Give the preparation type.
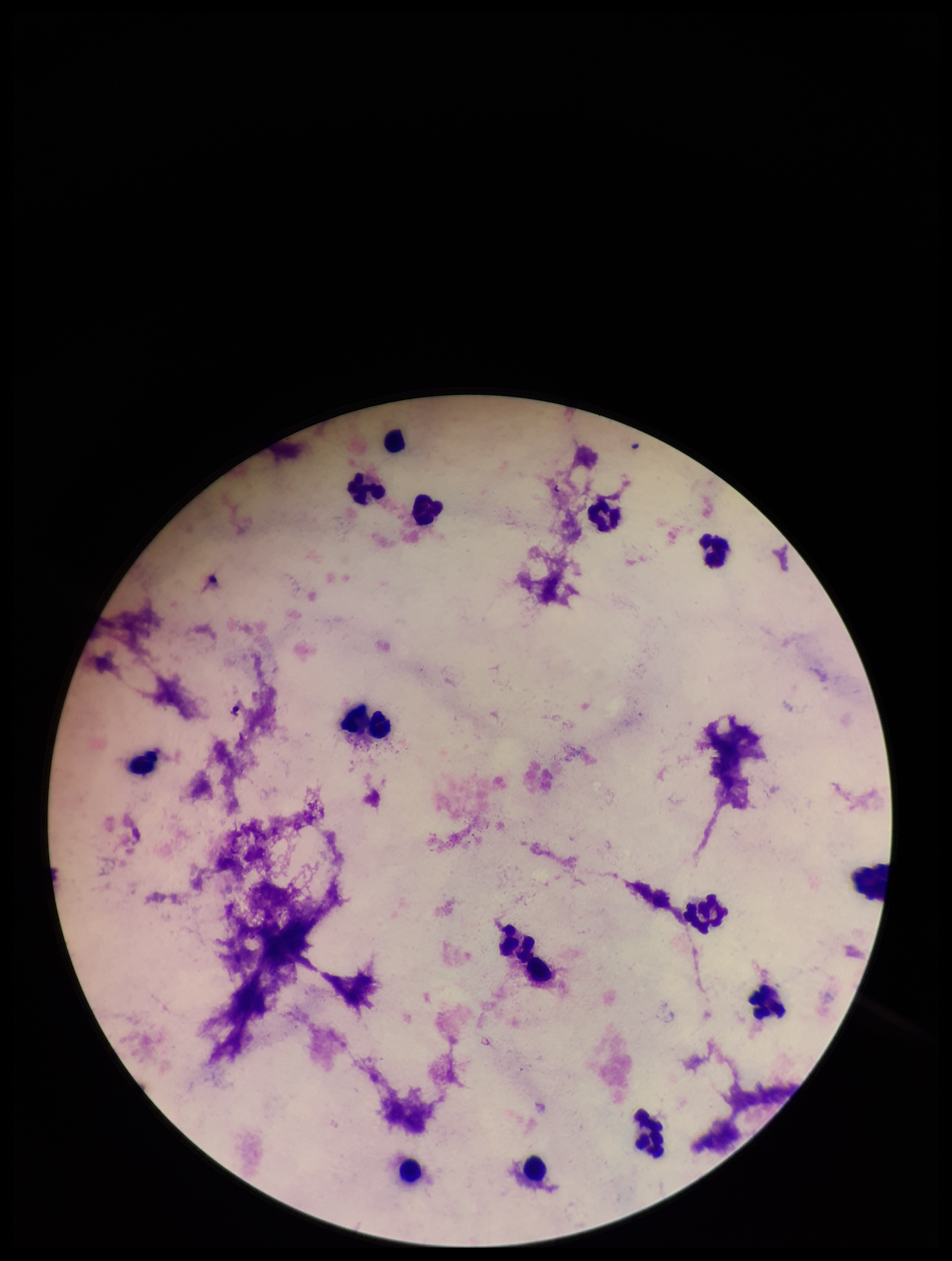

A thick smear.

Summary:
  - Image size: 952×1261 pixels
  - Field of view: single
  - Patient malaria status: negative
  - Leukocyte count: 13
  - Parasite count: 0
  - Plasmodium parasites: none detected
  - Capture: smartphone photograph through the microscope eyepiece
  - Stain: Giemsa